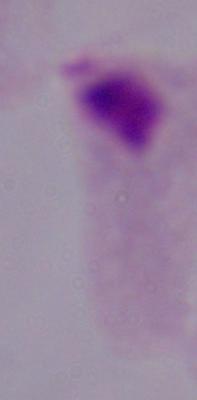
magnification = 1000x
identification = trichomonad
modality = photomicrograph